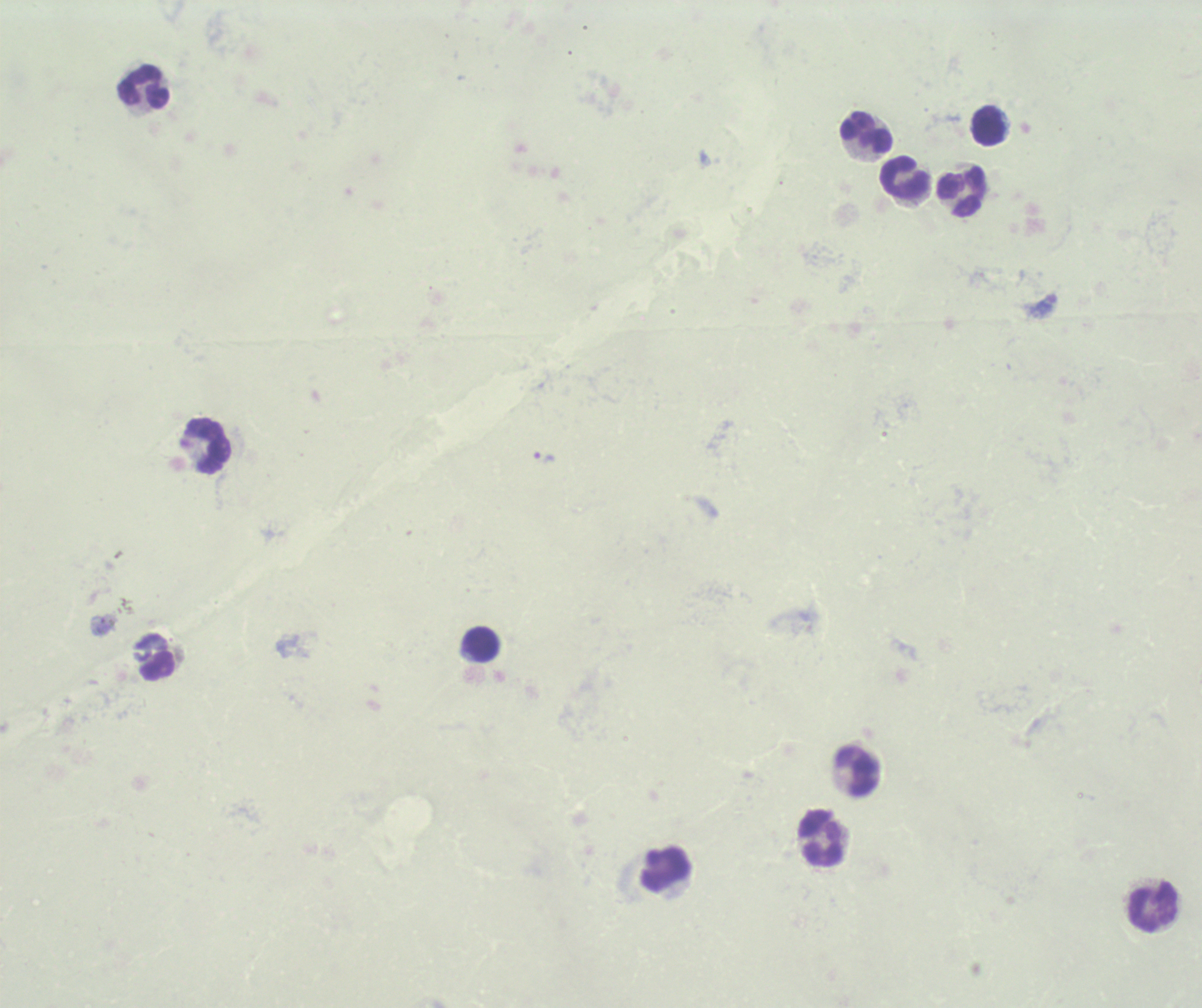

coordinate format = approximate centers as {x, y} in pixels
trophozoite locations = {543, 458}
leukocyte locations = {145, 89}, {988, 126}, {867, 135}, {903, 179}, {960, 193}, {206, 445}, {480, 645}, {159, 666}, {858, 771}, {822, 838}, {664, 870}, {1154, 906}
stain = Romanowsky
image size = 1202×1008 pixels
preparation = thick smear of blood
field of view = one from this slide
background quality = unsatisfactory
result = positive for Plasmodium parasites
magnification = 100x
context = previously used in an actual diagnosis